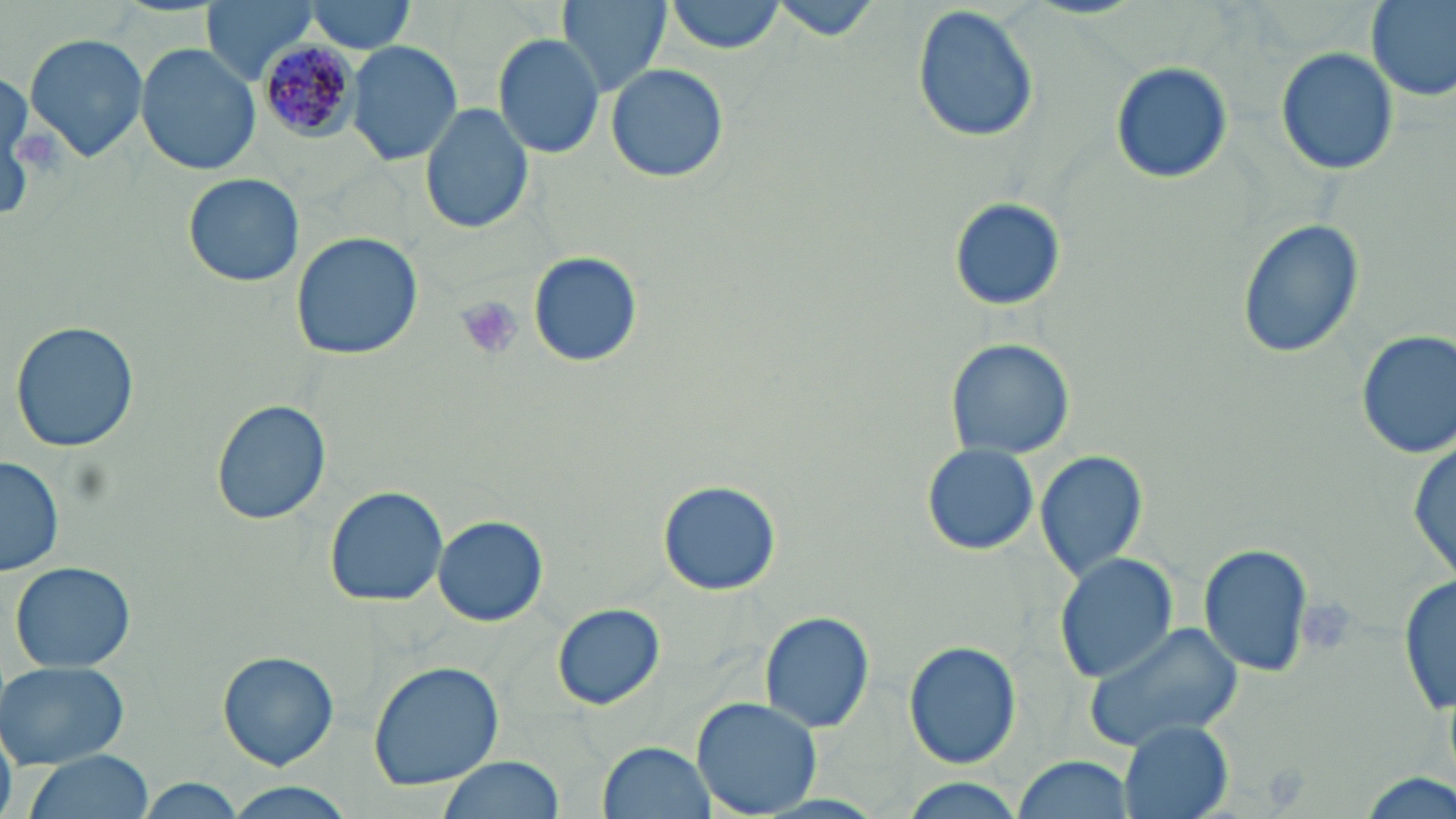

Approximate bounding boxes as (x1,y1)-(x2,y2) corner pairs in pixels. Uninfected red blood cell locations: (202,0)-(321,83), (303,0)-(416,55), (558,0)-(669,99), (667,0)-(786,55), (767,0)-(885,41), (1366,0)-(1456,104), (913,6)-(1041,143), (23,33)-(148,163), (494,33)-(606,159), (347,41)-(463,166), (134,43)-(259,177), (1276,46)-(1399,175), (1110,60)-(1233,184), (604,63)-(730,183), (421,100)-(534,234), (186,173)-(304,286), (950,197)-(1063,311), (1237,219)-(1363,359), (290,231)-(424,360), (528,252)-(644,367), (11,321)-(140,453), (1356,328)-(1456,461), (947,338)-(1073,459), (211,399)-(331,525), (1410,436)-(1454,589), (921,443)-(1039,556), (1035,449)-(1149,581), (1,454)-(65,576), (658,479)-(780,596), (324,487)-(451,607), (433,514)-(548,627), (1199,542)-(1314,678), (1053,553)-(1177,682), (10,561)-(135,674), (1398,567)-(1452,721), (553,603)-(664,709), (758,610)-(874,734), (1082,619)-(1244,751), (905,642)-(1021,769), (219,652)-(338,769), (368,660)-(504,792), (0,661)-(129,768), (691,697)-(823,819), (1117,719)-(1234,819), (597,741)-(715,819), (20,750)-(155,819), (1014,754)-(1136,819), (435,755)-(564,819), (895,777)-(1030,819), (135,779)-(248,818), (221,784)-(355,818). Plasmodium malariae-infected red blood cell locations: (256,39)-(357,140). Platelet locations: (11,124)-(68,175), (456,296)-(524,362), (1296,593)-(1360,654). Slide-level diagnosis: Plasmodium malariae. Optical microscopy. 1000x magnification. Single field of view. Thin blood film. Image is 1456×819 pixels. May-Grünwald-Giemsa-stained preparation.